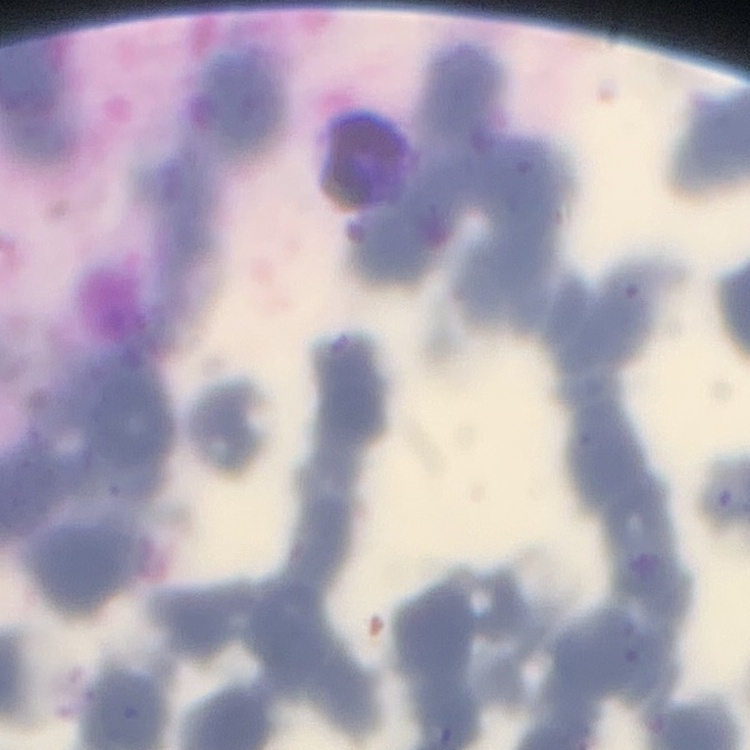

The erythrocytes show rouleaux formation. Square crop of a larger photomicrograph. Stained with either Field's or Giemsa. Thin blood film.